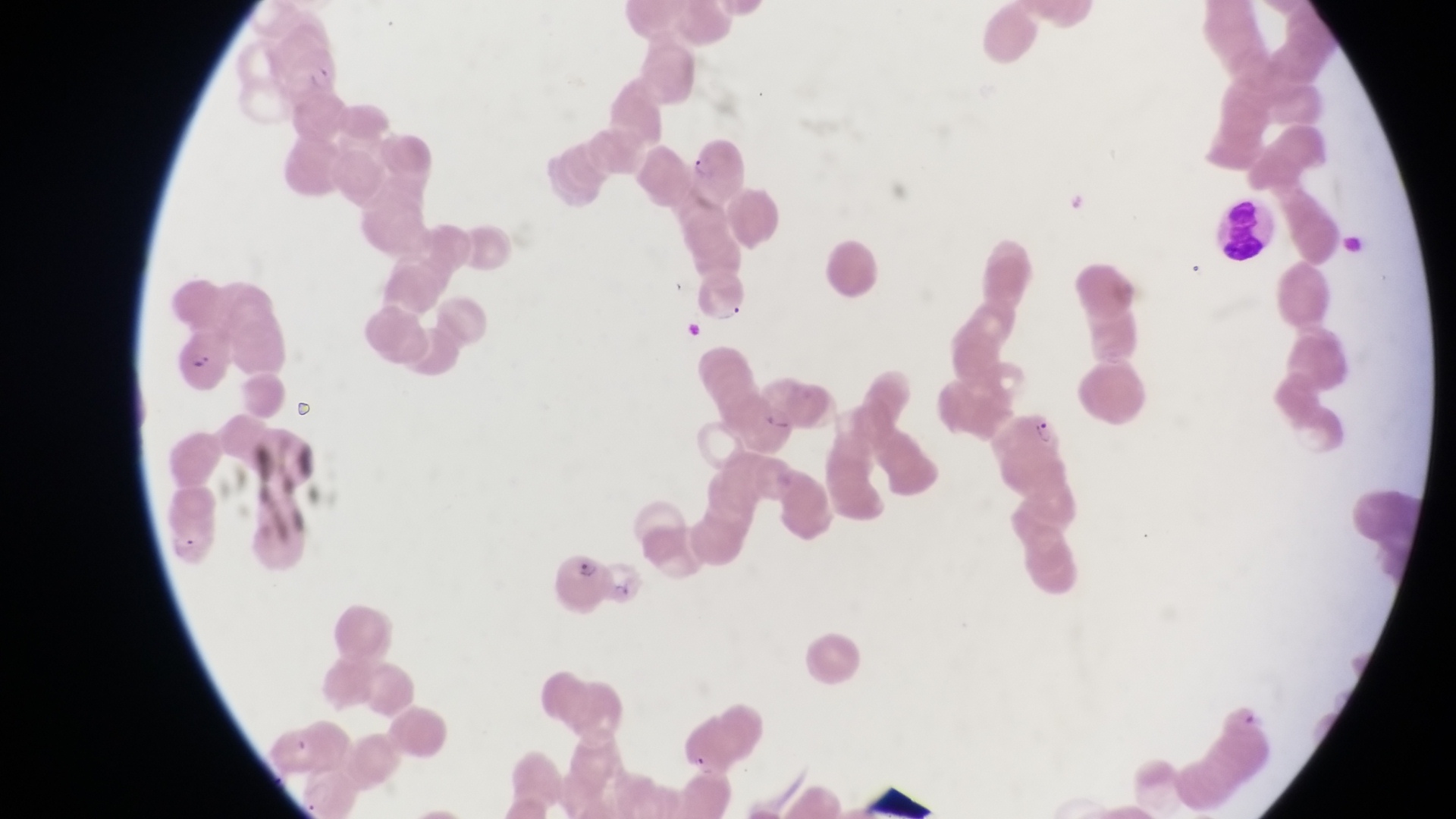
Approximate bounding boxes as [left, top, right, bottom] in pixels.
Summary:
  - Leukocyte locations: [1222, 199, 1277, 260]
  - Parasitised red blood cell locations: [272, 46, 343, 106], [682, 138, 745, 196], [171, 338, 231, 391], [999, 412, 1066, 475], [159, 512, 217, 571], [551, 549, 600, 604], [601, 560, 651, 609]
  - Image size: 1456×819 pixels
  - Country: Uganda
  - Preparation: thin blood smear
  - Magnification: 1000x
  - Field of view: single
  - Capture: smartphone photograph through the eyepiece of an Olympus CX-23 microscope